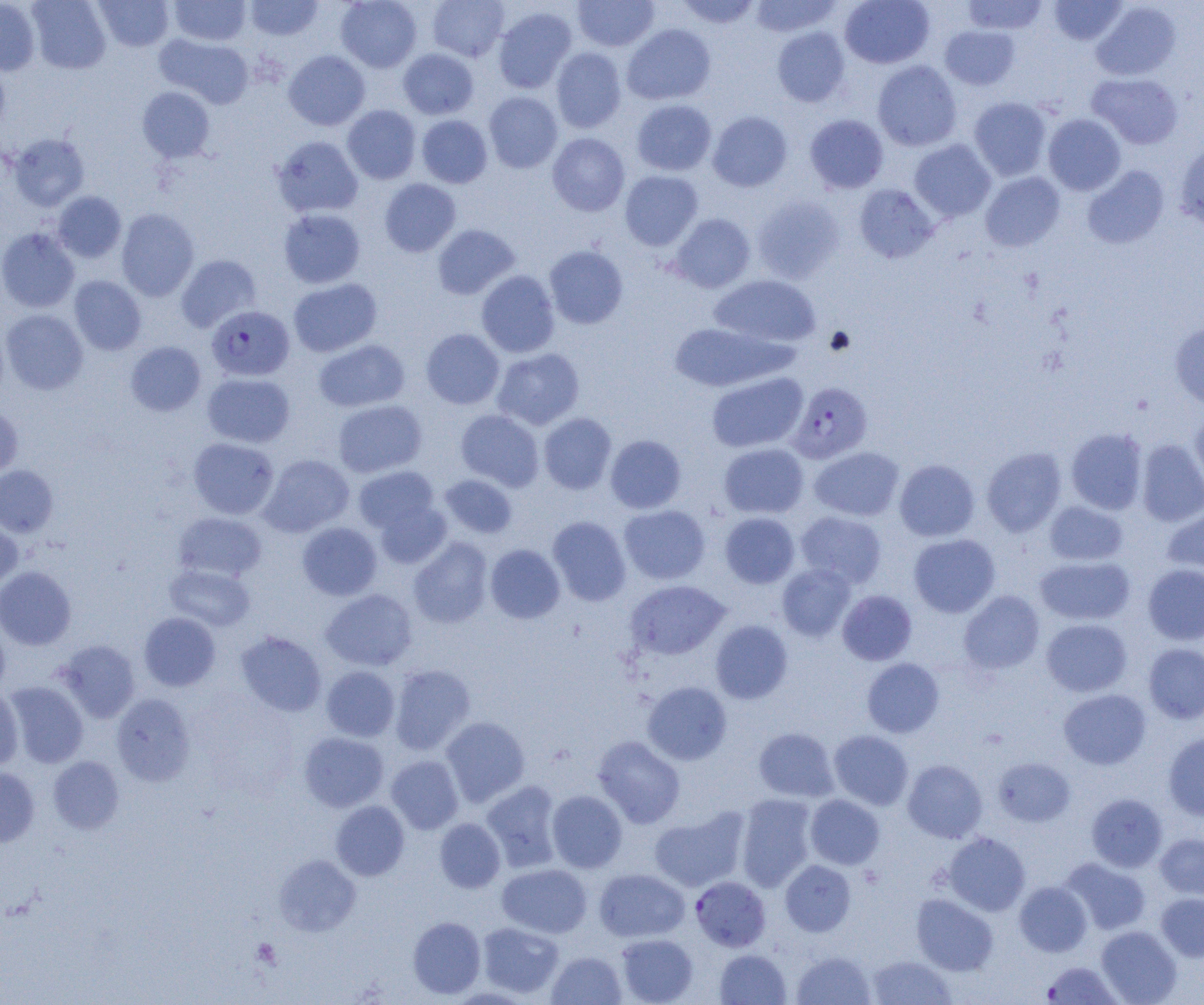 Approximate bounding boxes as [x1, y1, x2, y2] in pixels. Platelet locations: [252, 938, 282, 968]. Uninfected red blood cell locations: [28, 0, 110, 74], [93, 0, 173, 52], [169, 0, 251, 46], [245, 0, 323, 41], [336, 0, 421, 72], [427, 0, 509, 62], [572, 0, 659, 51], [675, 0, 761, 29], [748, 0, 842, 38], [839, 0, 934, 68], [962, 0, 1049, 35], [1048, 0, 1128, 46], [0, 1, 40, 75], [1091, 2, 1180, 81], [493, 6, 577, 94], [622, 23, 716, 105], [939, 25, 1021, 90], [772, 27, 851, 107], [155, 34, 253, 108], [550, 47, 627, 133], [398, 48, 479, 119], [283, 50, 370, 130], [872, 60, 962, 151], [0, 61, 10, 139], [1087, 72, 1183, 149], [138, 86, 215, 162], [484, 91, 563, 173], [968, 97, 1052, 181], [631, 99, 717, 176], [342, 105, 421, 184], [707, 111, 793, 192], [805, 114, 888, 193], [1042, 114, 1126, 196], [416, 115, 492, 188], [7, 133, 89, 211], [547, 133, 630, 216], [272, 135, 363, 218], [909, 139, 997, 222], [1175, 143, 1204, 230], [1082, 165, 1169, 249], [620, 170, 703, 251], [980, 172, 1065, 251], [379, 179, 461, 257], [854, 183, 939, 263], [53, 191, 126, 262], [753, 195, 845, 284], [116, 208, 199, 301], [278, 208, 365, 288], [668, 213, 756, 293], [432, 224, 520, 300], [0, 227, 80, 313], [544, 244, 629, 329], [176, 254, 261, 332], [476, 270, 560, 358], [709, 274, 821, 349], [69, 276, 146, 355], [288, 278, 382, 357], [2, 309, 88, 395], [668, 321, 793, 392], [1169, 323, 1204, 409], [421, 328, 505, 409], [313, 339, 410, 412], [126, 341, 206, 416], [492, 348, 585, 430], [202, 372, 295, 448], [707, 372, 808, 453], [332, 399, 427, 477], [0, 405, 23, 478], [455, 409, 544, 492], [1190, 410, 1204, 492], [538, 412, 616, 494], [1065, 428, 1148, 515], [605, 435, 686, 514], [188, 437, 279, 519], [1137, 439, 1204, 526], [718, 442, 809, 518], [809, 446, 904, 521], [982, 447, 1066, 537], [259, 454, 354, 537], [894, 459, 980, 541], [0, 465, 58, 536], [353, 466, 440, 535], [439, 474, 517, 538], [374, 500, 451, 568], [1044, 500, 1128, 566], [619, 505, 710, 584], [1163, 506, 1204, 580], [795, 510, 887, 588], [173, 512, 267, 582], [719, 512, 800, 588], [0, 516, 23, 590], [547, 516, 631, 606], [297, 522, 382, 601], [909, 534, 1000, 617], [408, 537, 493, 628], [485, 544, 565, 623], [1035, 556, 1135, 625], [777, 563, 856, 641], [1143, 564, 1204, 645], [165, 565, 255, 631], [0, 566, 76, 650], [625, 579, 730, 660], [321, 589, 417, 671], [838, 590, 916, 665], [959, 590, 1045, 674], [139, 612, 221, 691], [1041, 618, 1132, 697], [710, 620, 793, 704], [0, 623, 10, 699], [235, 631, 326, 717], [55, 639, 140, 723], [1143, 643, 1204, 724], [862, 658, 944, 738], [389, 664, 476, 755], [321, 666, 400, 741], [643, 681, 732, 765], [5, 682, 88, 768], [0, 685, 23, 769], [1058, 689, 1151, 769], [111, 693, 195, 786], [441, 716, 530, 806], [753, 727, 839, 802], [829, 730, 914, 810], [299, 731, 389, 812], [1163, 732, 1204, 821], [593, 735, 685, 828], [385, 755, 463, 834], [48, 756, 125, 834], [993, 757, 1075, 826], [902, 759, 987, 843], [0, 767, 39, 847], [482, 781, 562, 872], [547, 790, 627, 873], [735, 793, 817, 891], [1086, 793, 1167, 872], [805, 794, 885, 869], [330, 800, 409, 881], [649, 807, 749, 892], [434, 818, 505, 893], [942, 832, 1031, 915], [1154, 833, 1204, 900], [274, 854, 361, 936], [1061, 857, 1152, 935], [780, 860, 856, 936], [497, 863, 592, 938], [594, 868, 690, 942], [1014, 880, 1092, 956], [1155, 892, 1204, 962], [911, 894, 998, 975], [408, 916, 485, 999], [477, 921, 564, 998], [1096, 925, 1182, 1005], [616, 933, 698, 1005], [714, 949, 791, 1005], [791, 950, 876, 1005], [546, 951, 626, 1005], [867, 955, 957, 1004], [1041, 961, 1124, 1004]. Plasmodium falciparum-infected red blood cell locations: [206, 305, 294, 381], [788, 381, 872, 464], [691, 876, 771, 952]. Slide-level diagnosis: Plasmodium falciparum. Image is 1204×1005 pixels. Optical microscopy. 1000x magnification. Single field of view. Thin blood smear.